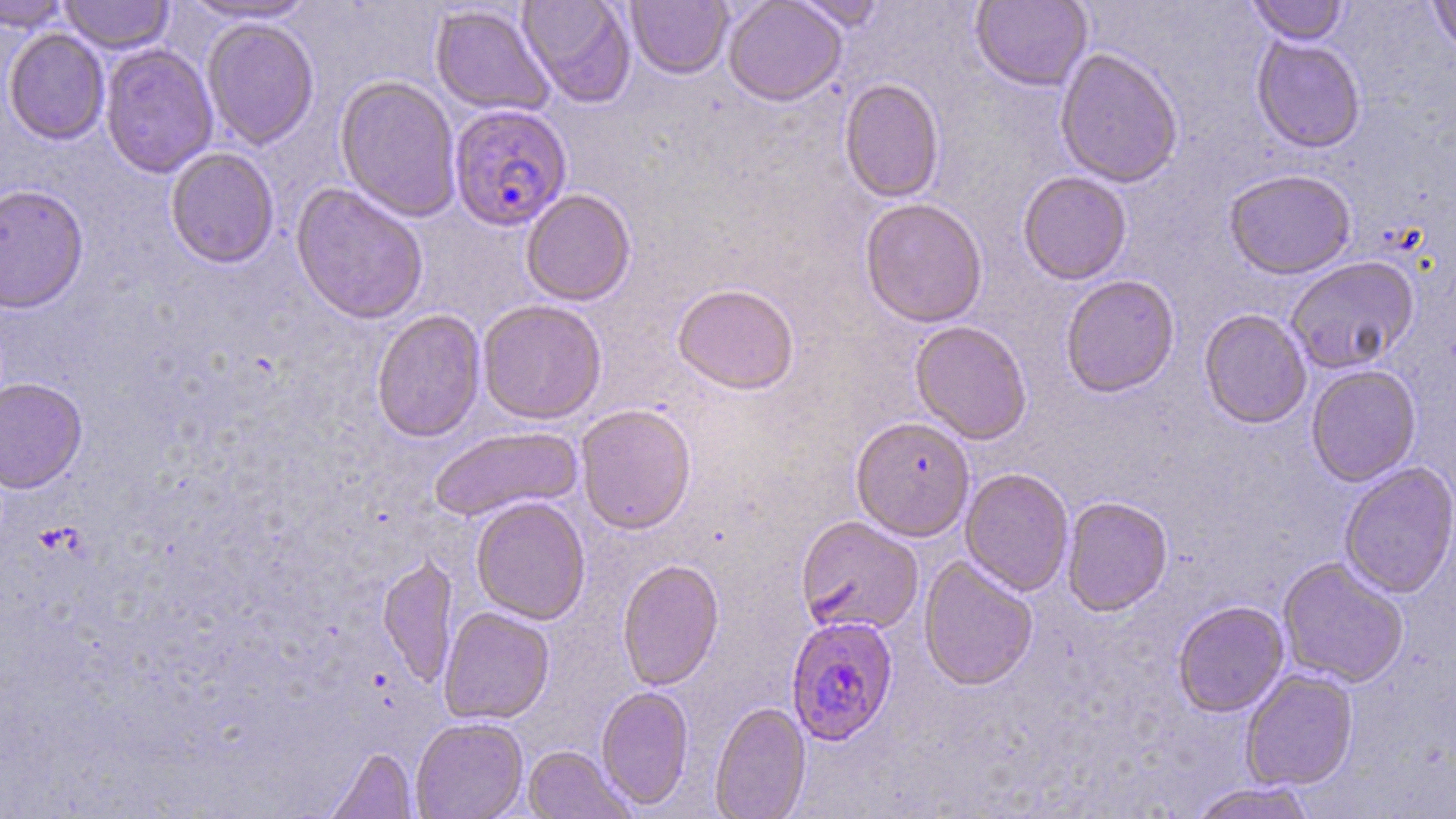
Approximate bounding boxes as [x1, y1, x2, y2] in pixels. Plasmodium falciparum-infected red blood cell locations: [449, 104, 572, 232], [785, 616, 899, 745]. Uninfected red blood cell locations: [0, 0, 72, 31], [59, 0, 175, 54], [179, 0, 320, 24], [517, 0, 636, 107], [625, 0, 734, 79], [722, 0, 847, 106], [790, 0, 888, 31], [1246, 0, 1350, 45], [1427, 0, 1456, 60], [970, 1, 1092, 92], [430, 5, 555, 118], [202, 18, 319, 149], [3, 28, 110, 145], [1251, 36, 1366, 153], [99, 44, 218, 179], [1054, 48, 1184, 188], [335, 75, 461, 223], [838, 78, 945, 204], [165, 148, 280, 270], [1223, 170, 1356, 281], [1017, 172, 1132, 286], [290, 184, 429, 327], [0, 185, 89, 315], [520, 190, 636, 307], [859, 199, 988, 329], [1285, 258, 1420, 375], [1060, 275, 1180, 399], [672, 285, 799, 397], [477, 301, 607, 425], [1199, 309, 1312, 430], [371, 310, 486, 444], [910, 322, 1032, 446], [1306, 365, 1421, 487], [0, 378, 88, 495], [575, 405, 696, 536], [850, 418, 975, 542], [428, 427, 582, 524], [1338, 463, 1456, 599], [959, 468, 1074, 596], [1062, 497, 1173, 616], [471, 498, 591, 625], [796, 517, 923, 636], [377, 556, 458, 689], [918, 556, 1038, 692], [1277, 558, 1409, 689], [617, 559, 724, 692], [1172, 601, 1289, 718], [438, 608, 555, 725], [1240, 669, 1359, 792], [596, 686, 694, 811], [710, 702, 811, 819], [410, 718, 528, 819], [523, 746, 634, 819], [324, 747, 418, 819], [1190, 782, 1318, 819]. Slide-level diagnosis: Plasmodium falciparum. May-Grünwald-Giemsa stain. 1000x magnification. Image is 1456×819 pixels. Single field of view. Light microscopy. Thin blood film.